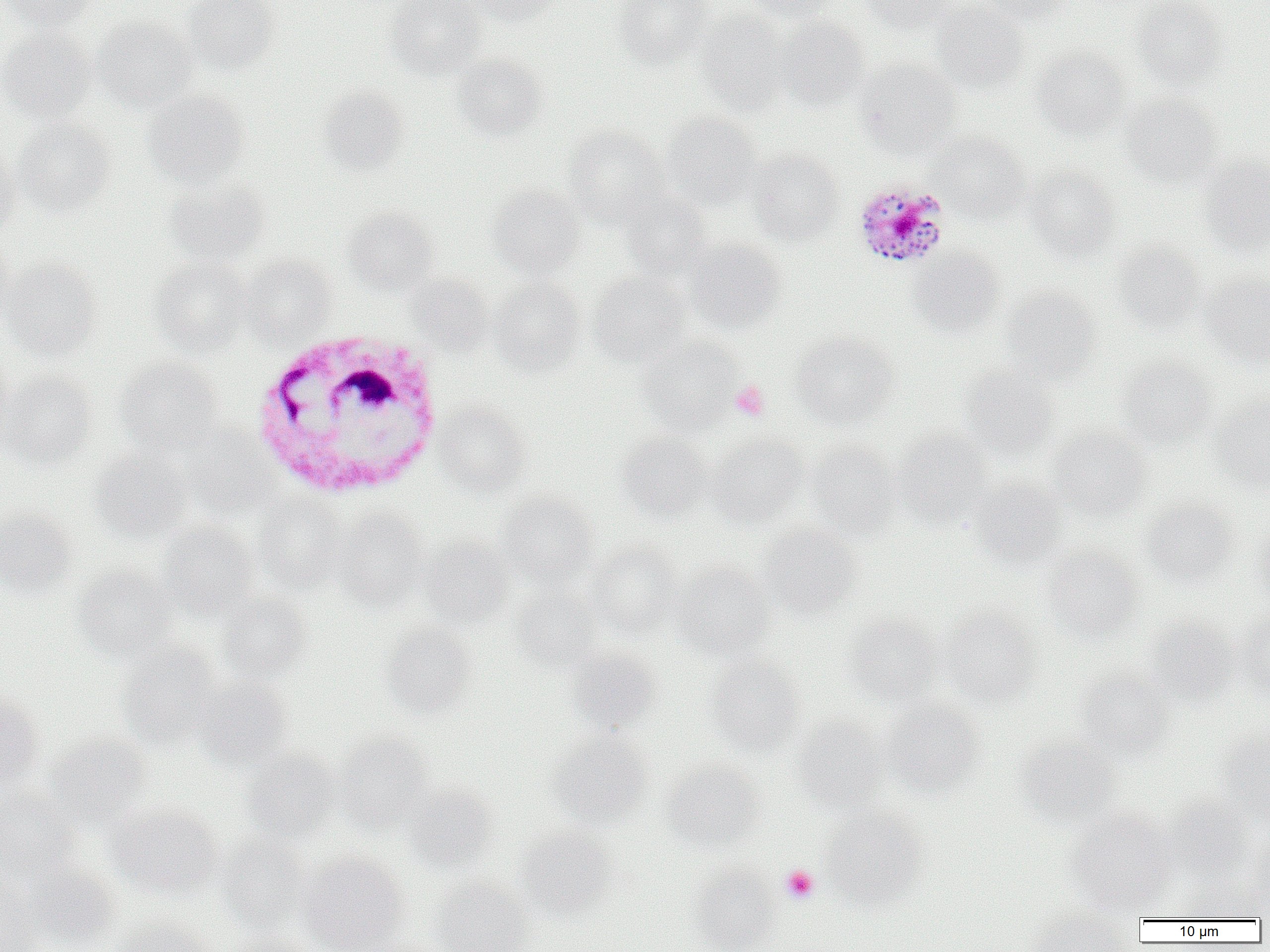

Approximate bounding boxes as (x1, y1, x2, y2) in pixels. Plasmodium malariae-infected red blood cell locations: (854, 179, 952, 268). White blood cell locations: (251, 328, 445, 499). Platelet locations: (730, 380, 770, 421), (781, 865, 819, 903). Uninfected red blood cell locations: (5, 0, 97, 31), (180, 0, 280, 75), (386, 0, 487, 80), (462, 0, 561, 26), (613, 0, 713, 68), (745, 0, 841, 21), (856, 0, 959, 32), (978, 0, 1072, 24), (1133, 0, 1229, 91), (931, 1, 1030, 95), (696, 11, 790, 113), (776, 16, 869, 111), (90, 17, 199, 111), (0, 27, 96, 121), (1032, 45, 1130, 139), (450, 53, 547, 141), (855, 59, 963, 160), (317, 85, 410, 176), (142, 88, 249, 188), (1120, 94, 1222, 188), (660, 112, 764, 211), (13, 118, 116, 216), (563, 125, 668, 225), (931, 132, 1030, 222), (0, 146, 21, 240), (747, 149, 844, 246), (1198, 152, 1270, 258), (1025, 165, 1120, 262), (164, 180, 270, 266), (487, 185, 586, 278), (617, 189, 713, 280), (343, 207, 439, 295), (0, 236, 16, 331), (685, 236, 787, 336), (1112, 242, 1205, 334), (907, 247, 1005, 338), (239, 255, 336, 343), (1, 257, 102, 359), (149, 257, 251, 356), (591, 269, 692, 367), (1200, 270, 1270, 368), (406, 274, 493, 354), (489, 278, 586, 376), (1003, 286, 1101, 383), (791, 332, 899, 429), (636, 336, 741, 433), (0, 347, 15, 454), (1115, 355, 1217, 449), (116, 356, 223, 454), (960, 365, 1059, 461), (0, 370, 97, 469), (1211, 397, 1270, 492), (434, 403, 530, 496), (187, 426, 277, 516), (1048, 426, 1150, 520), (893, 429, 992, 529), (617, 431, 713, 523), (706, 432, 808, 528), (806, 440, 902, 539), (91, 447, 192, 541), (971, 477, 1068, 568), (498, 491, 599, 587), (254, 495, 348, 592), (1141, 499, 1238, 588), (0, 508, 77, 596), (333, 508, 429, 608), (157, 521, 260, 618), (756, 522, 861, 619), (1250, 523, 1270, 611), (421, 537, 516, 628), (585, 540, 683, 639), (1042, 546, 1143, 642), (670, 561, 775, 660), (73, 566, 180, 662), (513, 584, 603, 671), (217, 591, 313, 684), (940, 606, 1040, 708), (1233, 609, 1270, 701), (844, 614, 942, 705), (1143, 617, 1238, 706), (380, 621, 478, 719), (118, 643, 223, 748), (564, 647, 662, 733), (705, 656, 805, 756), (1074, 669, 1174, 761), (194, 678, 294, 770), (0, 696, 45, 787), (880, 698, 987, 797), (793, 716, 889, 814), (1215, 724, 1270, 825), (546, 730, 652, 825), (335, 733, 433, 832), (47, 734, 153, 829), (1015, 736, 1121, 829), (243, 749, 340, 842), (662, 760, 764, 854), (403, 784, 499, 873), (0, 790, 81, 881), (1161, 797, 1256, 885), (106, 803, 221, 898), (820, 807, 928, 911), (1065, 808, 1178, 914), (515, 824, 617, 918), (1247, 834, 1270, 917), (217, 835, 311, 934), (300, 853, 408, 952), (22, 863, 121, 950), (688, 863, 780, 952), (0, 875, 43, 952), (1180, 877, 1267, 921), (431, 879, 530, 952), (1027, 906, 1134, 951), (109, 917, 213, 952), (231, 934, 321, 952). Slide-level diagnosis: Plasmodium malariae. Optical microscopy. Thin blood film. Captured at 1000x magnification. Single field of view. Image is 1270×952 pixels.